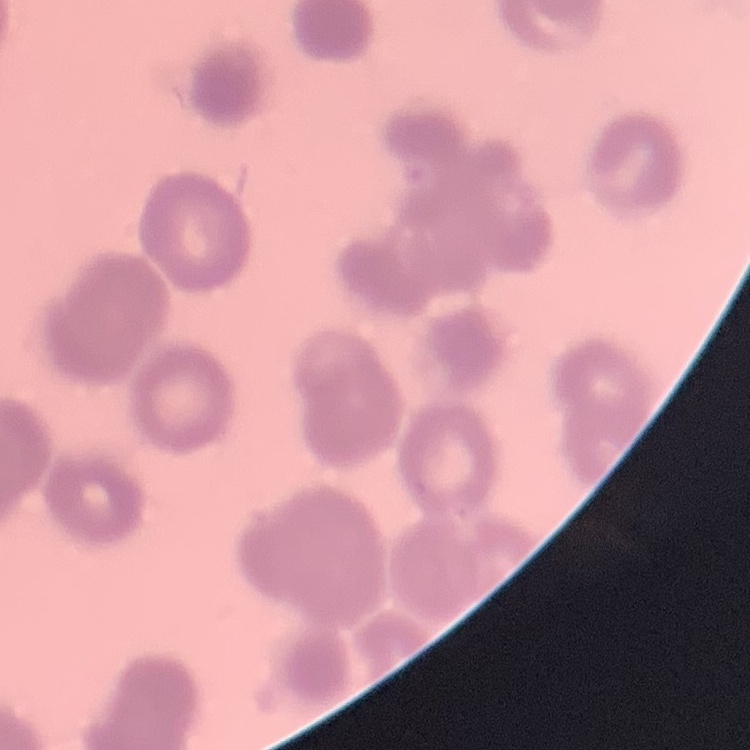

The erythrocytes exhibit rouleaux formation. Square crop of a larger photomicrograph. Stained with either Field's or Giemsa. Thin blood smear.